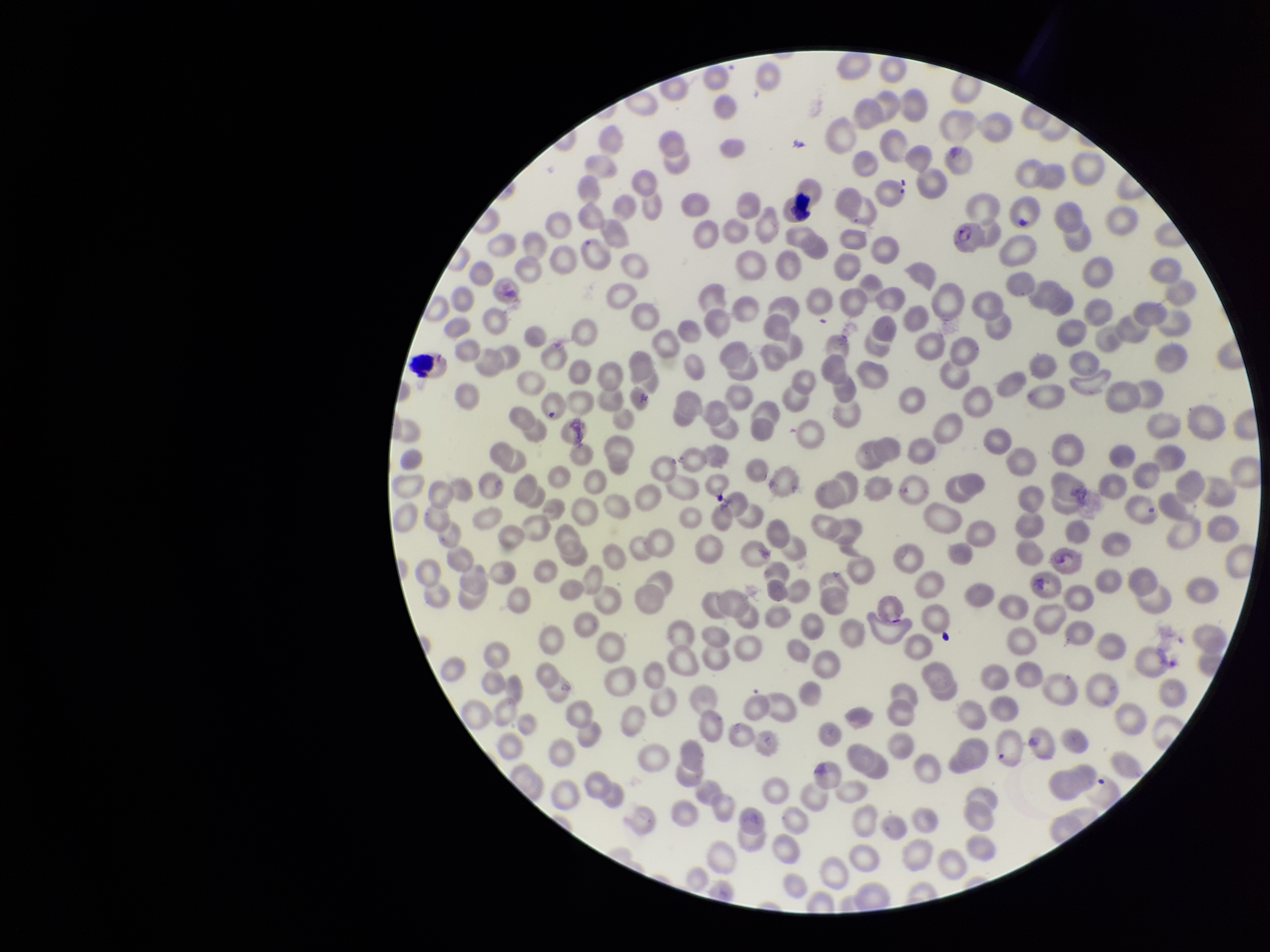
parasitized_red_blood_cells: seen
image_size: 1270×952 pixels
preparation: thin blood smear
patient_malaria_status: positive
capture: smartphone photograph through the microscope eyepiece
field_of_view: single
red_blood_cell_count: 305
species_reported_for_this_patient: Plasmodium falciparum
stain: Giemsa
parasitized_red_blood_cell_count: 2